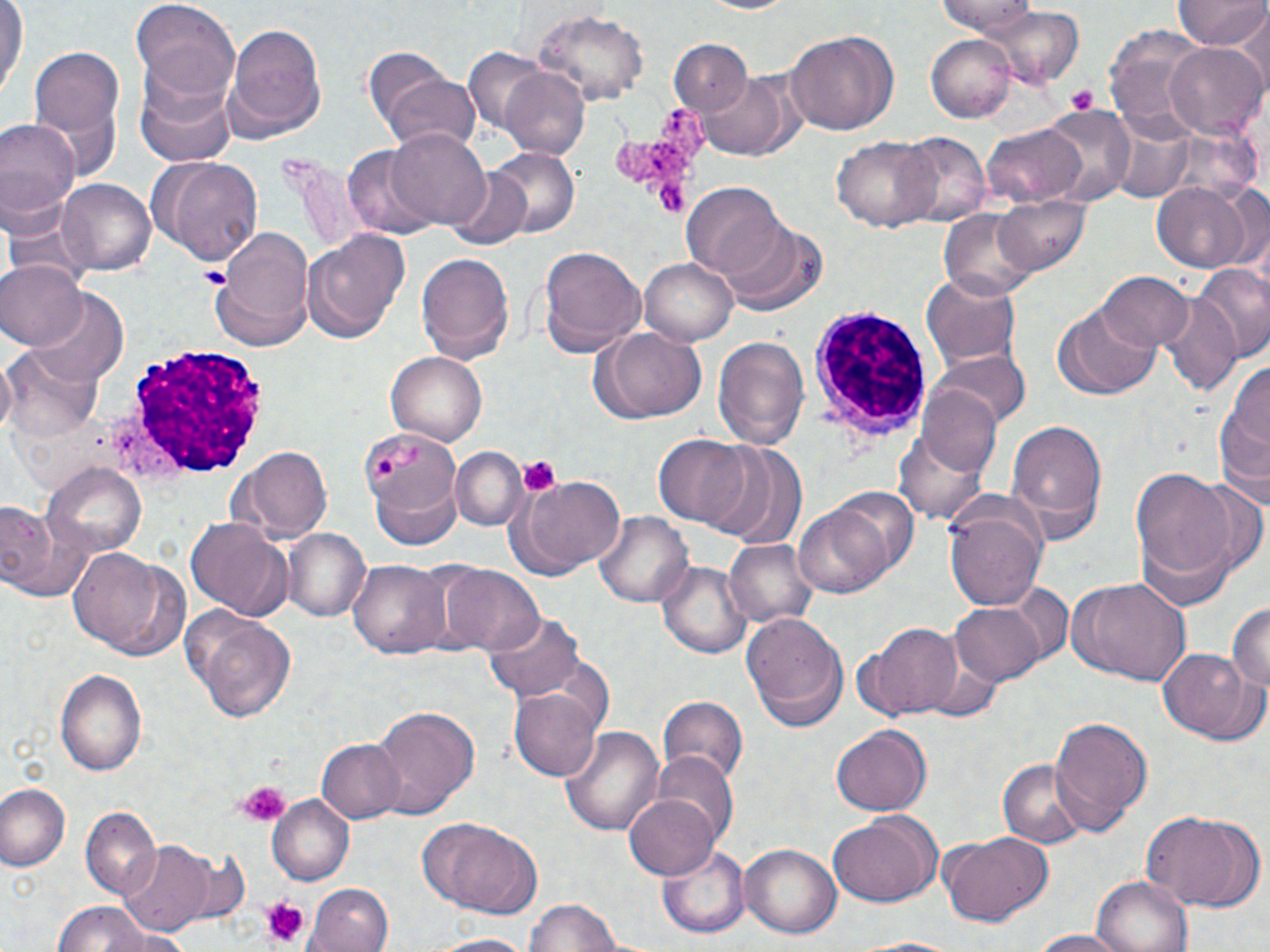

Summary:
  - Coordinate format: approximate bounding boxes as (x1,y1)-(x2,y2) corner pairs in pixels
  - Uninfected red blood cell locations: (697,0)-(802,16), (937,0)-(1040,34), (1172,1)-(1270,51), (0,2)-(27,98), (131,2)-(241,101), (533,9)-(648,108), (982,9)-(1086,85), (1233,12)-(1270,96), (221,17)-(328,138), (1104,27)-(1209,139), (787,29)-(900,135), (925,36)-(1015,121), (668,39)-(750,119), (1165,41)-(1266,141), (28,43)-(124,153), (462,50)-(552,133), (699,69)-(796,160), (500,70)-(590,159), (381,73)-(483,160), (134,74)-(239,172), (1039,105)-(1135,206), (0,115)-(80,234), (1110,123)-(1195,204), (982,126)-(1086,207), (385,128)-(490,230), (895,133)-(990,228), (833,134)-(941,232), (344,145)-(442,242), (485,148)-(580,240), (147,155)-(265,268), (285,155)-(368,256), (445,168)-(535,251), (56,178)-(158,280), (1154,183)-(1252,271), (683,184)-(787,282), (992,193)-(1091,275), (940,208)-(1040,301), (719,219)-(828,315), (208,226)-(312,352), (301,227)-(411,343), (538,245)-(646,360), (415,251)-(516,365), (640,256)-(737,344), (1192,261)-(1270,365), (0,262)-(86,352), (921,270)-(1024,373), (1096,271)-(1194,352), (25,290)-(129,388), (1156,293)-(1244,400), (1052,301)-(1162,402), (590,327)-(708,423), (711,333)-(811,450), (2,344)-(101,442), (386,348)-(487,445), (932,352)-(1030,433), (1214,354)-(1270,499), (919,382)-(1002,476), (1005,416)-(1106,535), (892,423)-(993,527), (654,434)-(755,529), (701,445)-(804,546), (231,447)-(334,542), (451,447)-(526,531), (41,461)-(149,560), (1126,466)-(1256,596), (510,475)-(627,578), (943,496)-(1048,609), (1,499)-(79,599), (793,500)-(895,599), (594,512)-(692,608), (185,517)-(291,620), (283,529)-(370,621), (724,538)-(817,629), (67,546)-(183,659), (349,560)-(451,659), (657,561)-(752,658), (445,567)-(545,656), (1065,577)-(1187,686), (1003,581)-(1073,667), (1227,601)-(1270,696), (949,602)-(1046,686), (186,612)-(298,723), (481,613)-(586,706), (743,613)-(849,731), (861,621)-(965,719), (1160,646)-(1257,742), (56,669)-(147,778), (512,688)-(604,781), (658,699)-(749,787), (369,705)-(480,816), (1050,717)-(1152,830), (559,725)-(664,835), (831,727)-(930,815), (318,740)-(402,821), (649,753)-(738,847), (998,757)-(1087,849), (1,784)-(69,871), (624,793)-(720,879), (266,795)-(355,886), (81,806)-(161,901), (1141,809)-(1263,911), (827,814)-(939,906), (417,819)-(543,919), (937,831)-(1051,927), (118,840)-(212,936), (739,841)-(842,938), (657,845)-(751,939), (1092,876)-(1194,952), (307,882)-(394,951), (526,896)-(624,952), (52,901)-(153,951), (108,929)-(194,952), (1030,930)-(1131,952), (425,934)-(542,952), (850,936)-(972,952)
  - Platelet locations: (1067,82)-(1100,114), (617,107)-(705,179), (649,175)-(691,220), (196,266)-(228,287), (371,456)-(398,481), (517,457)-(562,497), (236,783)-(290,827), (261,895)-(309,947)
  - White blood cell locations: (810,304)-(932,444), (123,343)-(269,479)
  - Slide-level diagnosis: Plasmodium malariae
  - Preparation: thin blood smear
  - Field of view: one of a larger specimen
  - Image size: 1270×952 pixels
  - Stain: May-Grünwald-Giemsa
  - Modality: optical microscopy
  - Magnification: 1000x